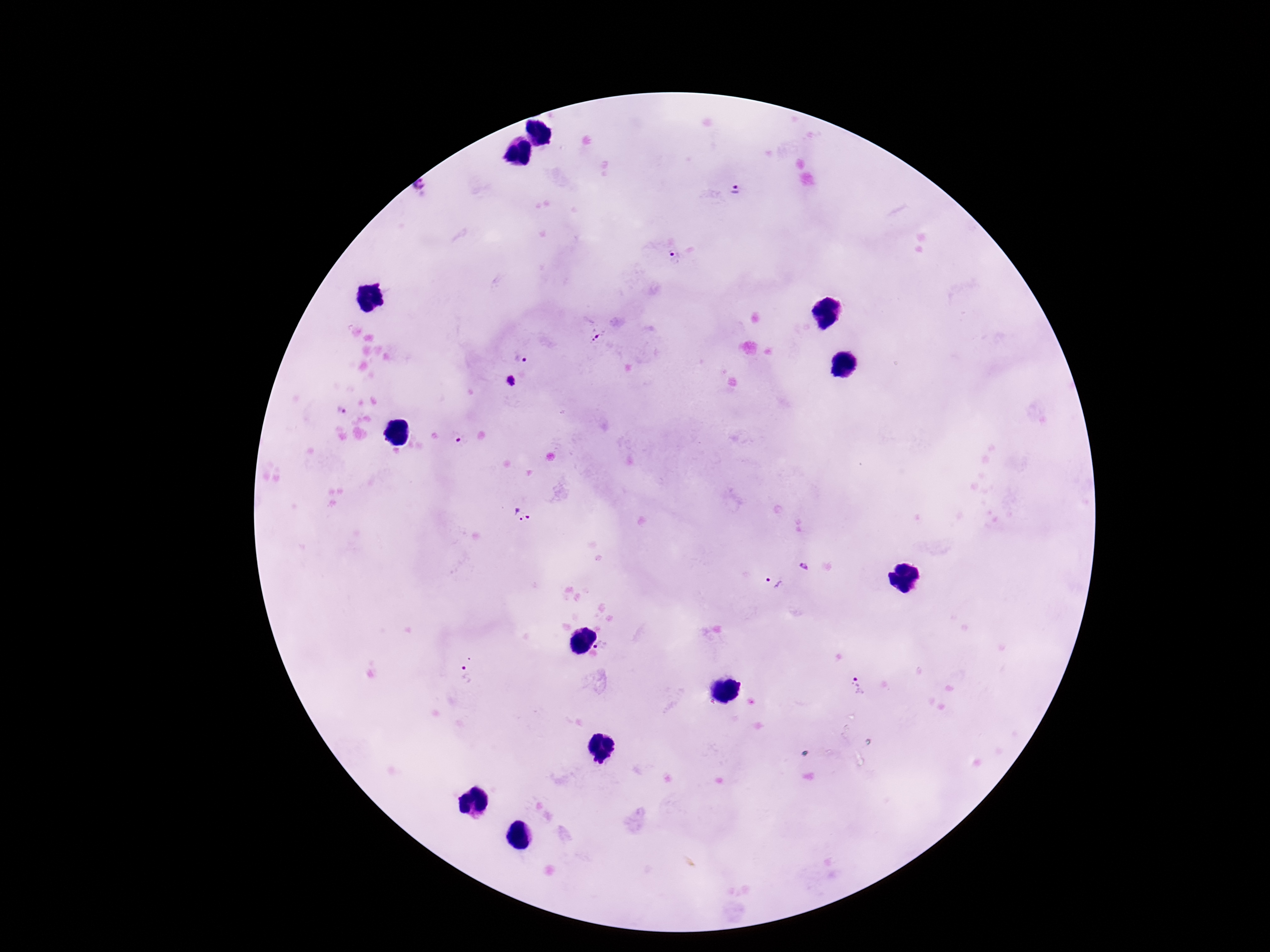 Approximate object centers, in pixels from the top-left corner. Plasmodium parasite locations: (x=420, y=189), (x=735, y=190), (x=673, y=255), (x=598, y=336), (x=521, y=359), (x=511, y=381), (x=340, y=411), (x=460, y=440), (x=522, y=514), (x=803, y=567), (x=773, y=583), (x=602, y=647), (x=465, y=675), (x=859, y=686). Smartphone photograph taken through the microscope eyepiece. Thick peripheral-blood smear. Image is 1270×952 pixels. Giemsa-stained preparation. One field from this slide. 100x magnification. Patient malaria status: positive.